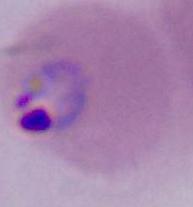

Captured at either 400x or 1000x magnification. A Plasmodium parasite is shown. Photomicrograph.